State which cell type is depicted.
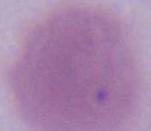
An erythrocyte.

{
  "magnification": "1000x",
  "modality": "micrograph"
}